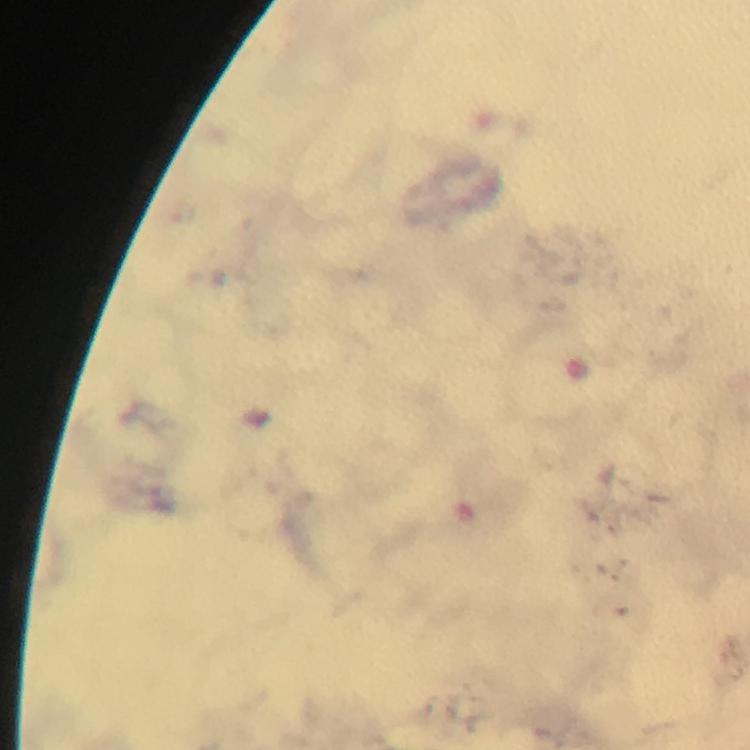
Approximate centers as (x, y) in pixels.
Summary:
  - Plasmodium parasite locations: (187, 213)
  - Image size: 750×750 pixels
  - Stain: Giemsa
  - Capture: smartphone mounted on the microscope
  - Preparation: thick smear
  - Magnification: 100x
  - Context: from a malaria diagnostic workup
  - Cropped from: one field of view
  - Immersion oil: used